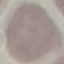

result = no malaria parasites seen
stain = Giemsa
capture = smartphone through the microscope eyepiece
preparation = thin blood film
image type = cell patch, automatically extracted from a larger field of view and resized to 64 × 64 pixels